Name the blood parasite species.
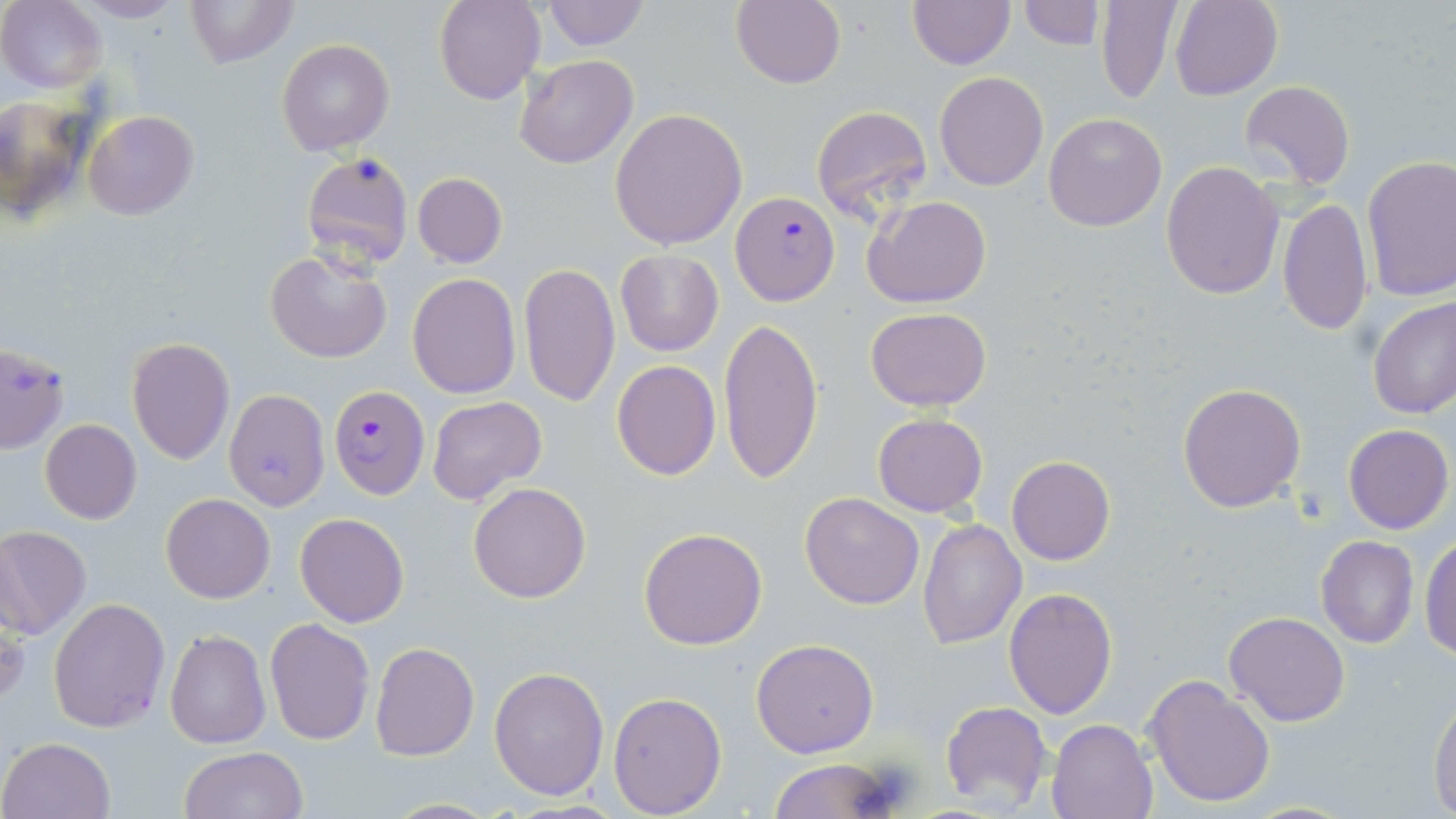
Plasmodium falciparum.

image size = 1456×819 pixels
magnification = 1000x
uninfected red blood cell locations = approximate bounding boxes as (x1,y1)-(x2,y2) corner pairs in pixels: (184,0)-(297,68), (434,0)-(545,104), (540,0)-(650,50), (731,0)-(845,89), (1018,0)-(1102,50), (1094,0)-(1183,103), (1,1)-(106,93), (72,1)-(186,23), (906,1)-(1014,69), (1168,1)-(1282,100), (276,38)-(394,154), (514,56)-(637,170), (934,72)-(1048,190), (1238,81)-(1355,189), (0,100)-(95,218), (810,104)-(934,227), (608,108)-(750,249), (83,109)-(198,219), (1043,112)-(1167,231), (302,152)-(415,271), (1360,155)-(1456,302), (1161,160)-(1284,299), (411,172)-(508,268), (863,195)-(990,307), (1278,196)-(1373,336), (265,248)-(393,364), (615,249)-(723,356), (518,262)-(620,407), (408,273)-(522,398), (1368,295)-(1456,420), (865,307)-(991,412), (719,315)-(825,487), (125,336)-(235,466), (0,341)-(69,454), (612,359)-(720,479), (1177,382)-(1308,513), (224,388)-(330,510), (426,395)-(548,506), (872,412)-(988,518), (39,419)-(143,524), (1343,424)-(1453,534), (1007,455)-(1115,565), (468,482)-(592,603), (800,493)-(924,609), (160,494)-(275,604), (295,513)-(409,627), (917,518)-(1027,650), (0,525)-(91,638), (638,527)-(767,649), (1420,533)-(1456,660), (1315,535)-(1419,648), (1004,586)-(1118,721), (48,598)-(170,732), (0,601)-(26,708), (1224,610)-(1349,727), (265,617)-(375,744), (164,629)-(271,748), (750,638)-(878,757), (370,642)-(479,762), (489,664)-(609,801), (1144,673)-(1275,810), (607,691)-(727,816), (1428,694)-(1456,814), (939,700)-(1053,812), (1047,717)-(1160,819), (0,736)-(115,818), (179,746)-(308,819), (768,758)-(895,818), (380,798)-(503,818)
stain = May-Grünwald-Giemsa
Plasmodium falciparum-infected red blood cell locations = approximate bounding boxes as (x1,y1)-(x2,y2) corner pairs in pixels: (730,192)-(839,306), (328,383)-(429,499)
field of view = one of a larger specimen
preparation = thin blood film
modality = optical microscopy